Assess this cell for malaria.
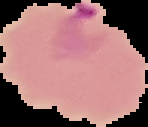
It is parasitized.

Summary:
  - Preparation: thin blood film
  - Image type: segmented cell region with the area outside set to black
  - Image size: 148×127 pixels